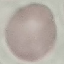
malaria status = uninfected
capture = smartphone camera at the microscope eyepiece
stain = Giemsa
image type = cell patch, automatically extracted from a larger field of view and resized to 64 × 64 pixels
preparation = thin blood film